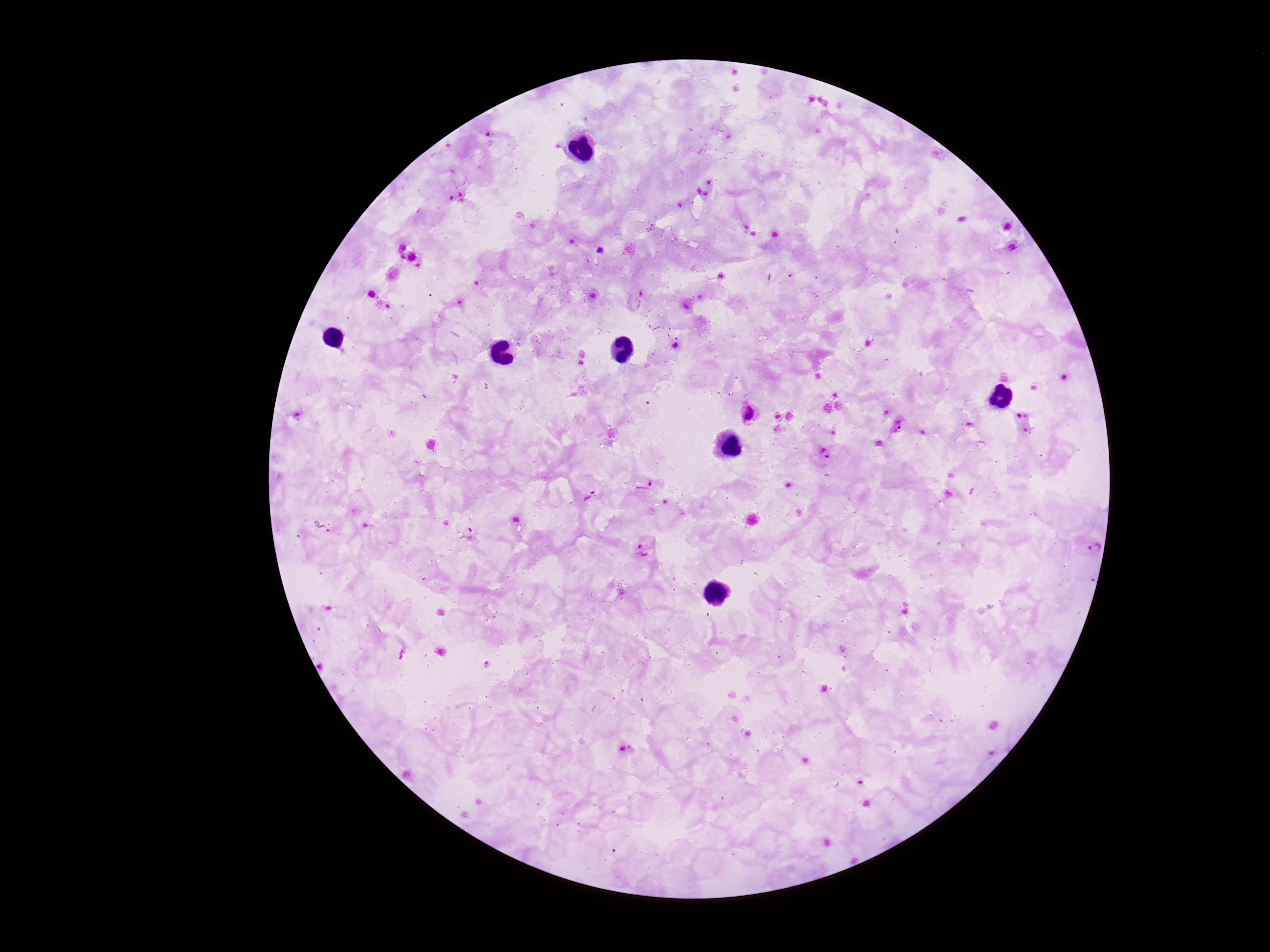
magnification = 100x
patient malaria status = positive
field of view = single
Plasmodium parasite locations = approximate centers as (x, y) in pixels: (896, 236), (600, 251), (655, 322), (675, 333), (583, 353), (581, 364), (1021, 413), (749, 414), (895, 426), (1027, 430), (826, 455), (642, 483), (589, 495), (321, 527), (468, 535), (645, 550)
preparation = thick peripheral-blood smear
stain = Giemsa
capture = smartphone camera through the microscope eyepiece
image size = 1270×952 pixels